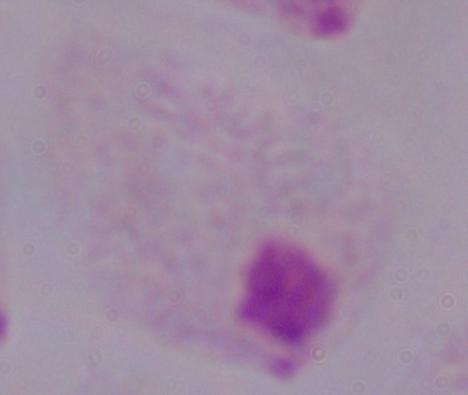
A trichomonad is shown. Micrograph. 1000x magnification.